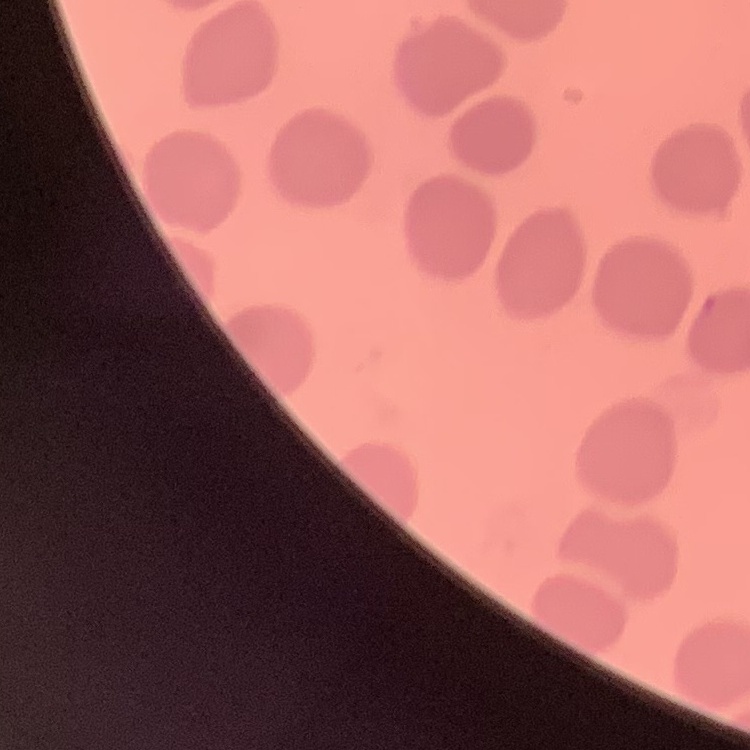

The red blood cells show no rouleaux formation. Square crop of a larger photomicrograph. Thin blood film. Field's or Giemsa stain.